Outline each uninfected red blood cell.
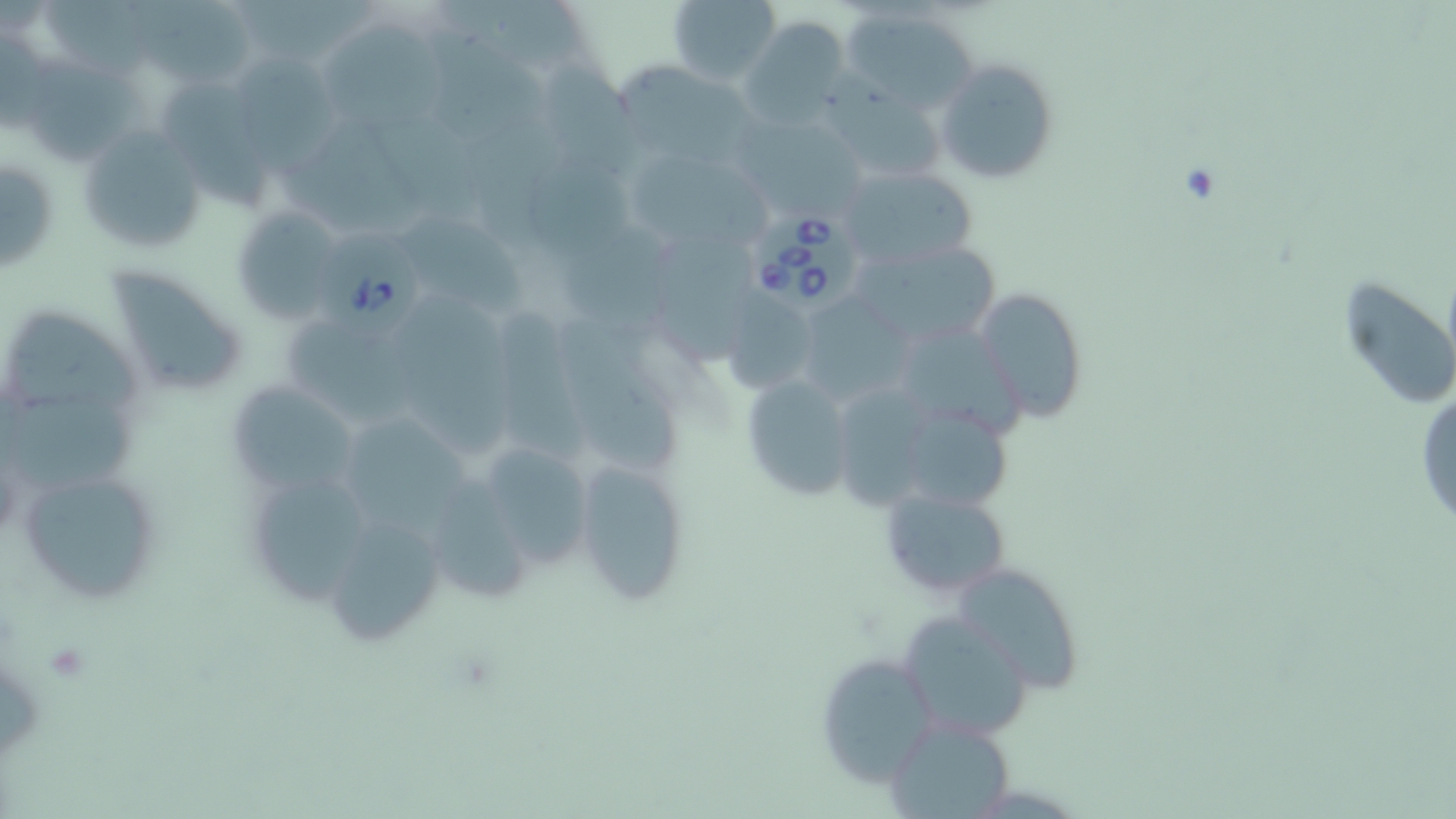
Approximate bounding boxes as [x1, y1, x2, y2] in pixels.
Uninfected red blood cells: [667, 0, 779, 86], [46, 1, 171, 79], [438, 1, 595, 82], [127, 3, 258, 83], [839, 4, 977, 113], [740, 15, 852, 127], [322, 16, 456, 134], [228, 54, 336, 167], [936, 58, 1060, 183], [28, 63, 152, 168], [616, 65, 768, 172], [165, 84, 277, 220], [823, 84, 949, 185], [743, 118, 869, 216], [75, 123, 208, 257], [626, 152, 775, 245], [1, 155, 57, 275], [837, 163, 980, 272], [231, 205, 343, 325], [409, 224, 528, 319], [562, 232, 695, 353], [652, 236, 769, 370], [851, 239, 1004, 346], [106, 265, 247, 396], [1337, 277, 1456, 403], [973, 286, 1090, 423], [717, 289, 824, 396], [401, 298, 521, 462], [12, 313, 153, 416], [499, 313, 601, 463], [556, 317, 692, 477], [904, 326, 1035, 447], [739, 372, 858, 503], [226, 379, 363, 498], [834, 384, 951, 513], [1415, 388, 1456, 532], [5, 396, 146, 498], [905, 413, 1020, 513], [342, 416, 481, 532], [469, 438, 598, 576], [573, 456, 690, 608], [17, 465, 162, 604], [420, 478, 537, 610], [879, 486, 1011, 600], [325, 514, 447, 644], [952, 559, 1087, 693], [898, 609, 1035, 741], [812, 649, 938, 785], [883, 714, 1017, 818].

Babesia divergens-infected red blood cell locations: [747, 213, 866, 311], [313, 235, 421, 336]. Platelet locations: [42, 641, 91, 681]. Slide-level diagnosis: Babesia divergens. May-Grünwald-Giemsa stain. Single field of view. Image is 1456×819 pixels. Thin blood smear. Light microscopy. Captured at 1000x magnification.